Name the blood parasite species.
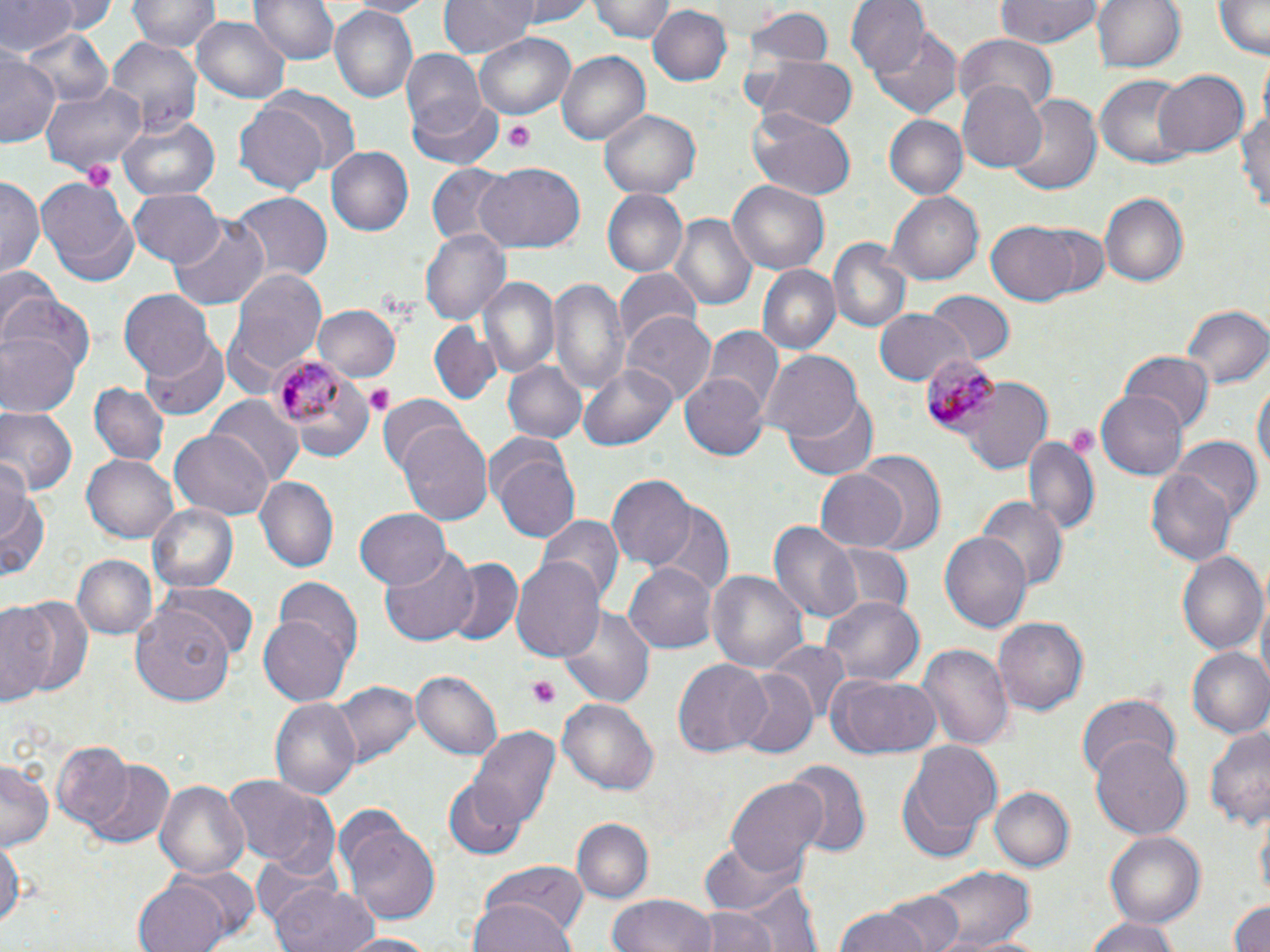

Plasmodium malariae.

Approximate bounding boxes as (x1, y1, x2, y2) in pixels. Plasmodium malariae-infected red blood cell locations: (269, 350, 345, 430), (920, 353, 1000, 434). Uninfected red blood cell locations: (14, 0, 115, 40), (130, 0, 218, 53), (252, 0, 338, 66), (344, 0, 436, 17), (438, 0, 540, 56), (506, 0, 598, 25), (592, 0, 675, 43), (847, 0, 926, 76), (994, 0, 1099, 49), (1091, 0, 1185, 74), (0, 1, 80, 57), (1214, 2, 1268, 59), (648, 4, 731, 85), (328, 7, 418, 103), (742, 7, 833, 70), (191, 17, 290, 103), (870, 23, 963, 118), (19, 27, 112, 111), (954, 33, 1057, 113), (105, 35, 203, 140), (476, 35, 575, 117), (0, 41, 59, 151), (557, 49, 650, 147), (402, 51, 484, 132), (755, 55, 857, 132), (1153, 68, 1250, 157), (1093, 73, 1194, 171), (41, 79, 148, 178), (959, 84, 1047, 172), (407, 95, 505, 171), (1008, 95, 1101, 198), (1238, 95, 1270, 216), (234, 101, 330, 193), (600, 107, 699, 199), (748, 114, 854, 201), (119, 115, 219, 202), (882, 115, 968, 198), (326, 146, 414, 235), (476, 161, 585, 251), (425, 163, 514, 247), (34, 173, 139, 280), (1, 179, 42, 279), (729, 181, 829, 273), (129, 189, 226, 265), (602, 189, 686, 277), (229, 191, 333, 282), (1101, 191, 1189, 288), (888, 193, 982, 282), (168, 215, 273, 308), (672, 215, 757, 311), (987, 221, 1081, 305), (1030, 223, 1113, 303), (421, 228, 510, 323), (828, 238, 913, 334), (756, 265, 839, 354), (0, 266, 59, 332), (224, 268, 329, 395), (614, 270, 703, 353), (480, 277, 559, 381), (549, 278, 629, 393), (119, 288, 214, 378), (0, 291, 95, 377), (925, 293, 1013, 365), (312, 304, 402, 382), (1179, 304, 1268, 391), (872, 307, 970, 388), (622, 312, 717, 405), (429, 322, 500, 405), (705, 328, 781, 414), (0, 331, 80, 418), (141, 336, 232, 420), (758, 348, 865, 443), (1121, 352, 1214, 435), (503, 360, 587, 445), (578, 365, 674, 452), (679, 371, 769, 461), (1251, 374, 1269, 488), (962, 379, 1055, 474), (90, 383, 167, 468), (1098, 388, 1191, 479), (785, 394, 877, 481), (207, 396, 305, 485), (379, 396, 467, 480), (0, 407, 77, 500), (396, 422, 493, 525), (166, 429, 275, 521), (1022, 432, 1098, 537), (485, 437, 580, 547), (1169, 438, 1261, 524), (851, 452, 946, 554), (83, 454, 180, 543), (1, 455, 37, 546), (814, 468, 911, 553), (1148, 469, 1237, 566), (608, 475, 697, 570), (0, 476, 47, 583), (254, 477, 337, 570), (977, 498, 1067, 593), (148, 504, 240, 595), (650, 505, 734, 595), (355, 508, 451, 590), (537, 515, 622, 605), (769, 519, 862, 623), (942, 530, 1033, 631), (824, 544, 914, 618), (378, 546, 482, 647), (1177, 547, 1268, 655), (73, 555, 156, 641), (514, 556, 606, 661), (444, 557, 525, 646), (625, 561, 719, 655), (706, 569, 809, 675), (272, 578, 364, 678), (162, 582, 258, 658), (820, 595, 924, 688), (0, 599, 62, 709), (561, 605, 656, 708), (132, 608, 236, 704), (260, 612, 353, 708), (992, 613, 1088, 713), (765, 642, 850, 721), (918, 643, 1012, 753), (1186, 647, 1270, 739), (673, 658, 771, 759), (410, 668, 502, 760), (728, 670, 818, 758), (827, 676, 943, 759), (330, 680, 418, 767), (1077, 692, 1182, 782), (556, 695, 659, 794), (271, 700, 359, 797), (1206, 721, 1270, 835), (468, 723, 561, 834), (1089, 739, 1192, 839), (52, 741, 132, 831), (908, 743, 1003, 838), (78, 756, 177, 847), (1, 759, 53, 854), (786, 760, 870, 854), (221, 773, 334, 870), (155, 778, 250, 882), (726, 778, 827, 877), (445, 780, 526, 859), (990, 787, 1074, 873), (337, 812, 441, 925), (572, 817, 653, 904), (1105, 832, 1203, 927), (0, 833, 23, 939), (698, 839, 806, 923), (250, 858, 343, 937), (923, 862, 1035, 949), (477, 863, 588, 941), (719, 875, 824, 952), (133, 876, 235, 952), (267, 881, 378, 952), (885, 890, 964, 952), (608, 894, 715, 952), (468, 896, 577, 952), (1225, 896, 1270, 952), (686, 907, 782, 952), (832, 908, 934, 952), (1083, 916, 1184, 952), (340, 934, 445, 951). Platelet locations: (506, 122, 536, 150), (80, 159, 119, 192), (364, 384, 394, 415), (530, 676, 559, 709). Thin blood smear. One field of a larger specimen. Light microscopy. Image is 1270×952 pixels. May-Grünwald-Giemsa stain. Captured at 1000x magnification.